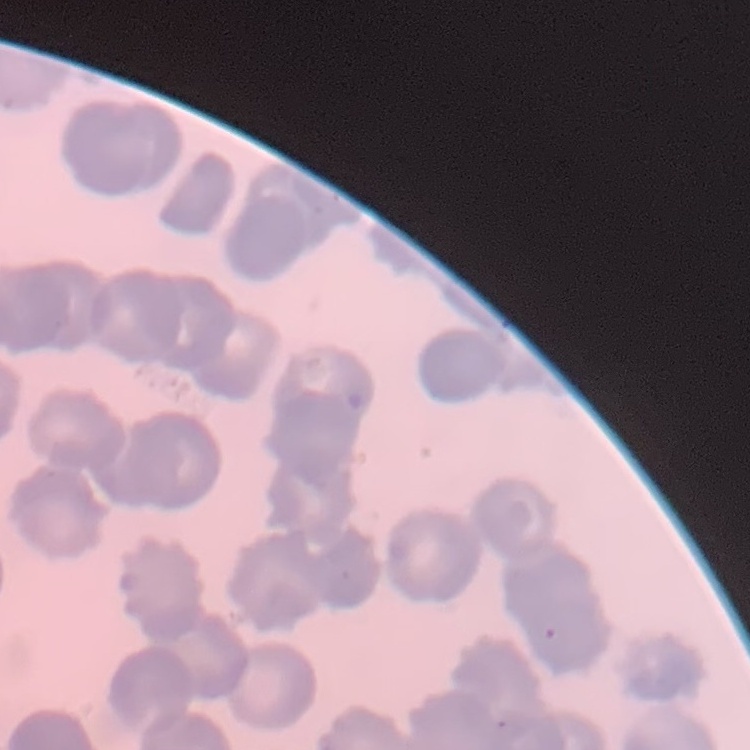
red blood cell morphology = rouleaux formation
image type = one tile cut from a larger photomicrograph
preparation = thin blood smear
stain = Field's or Giemsa